Locate every blood parasite and identify its species.
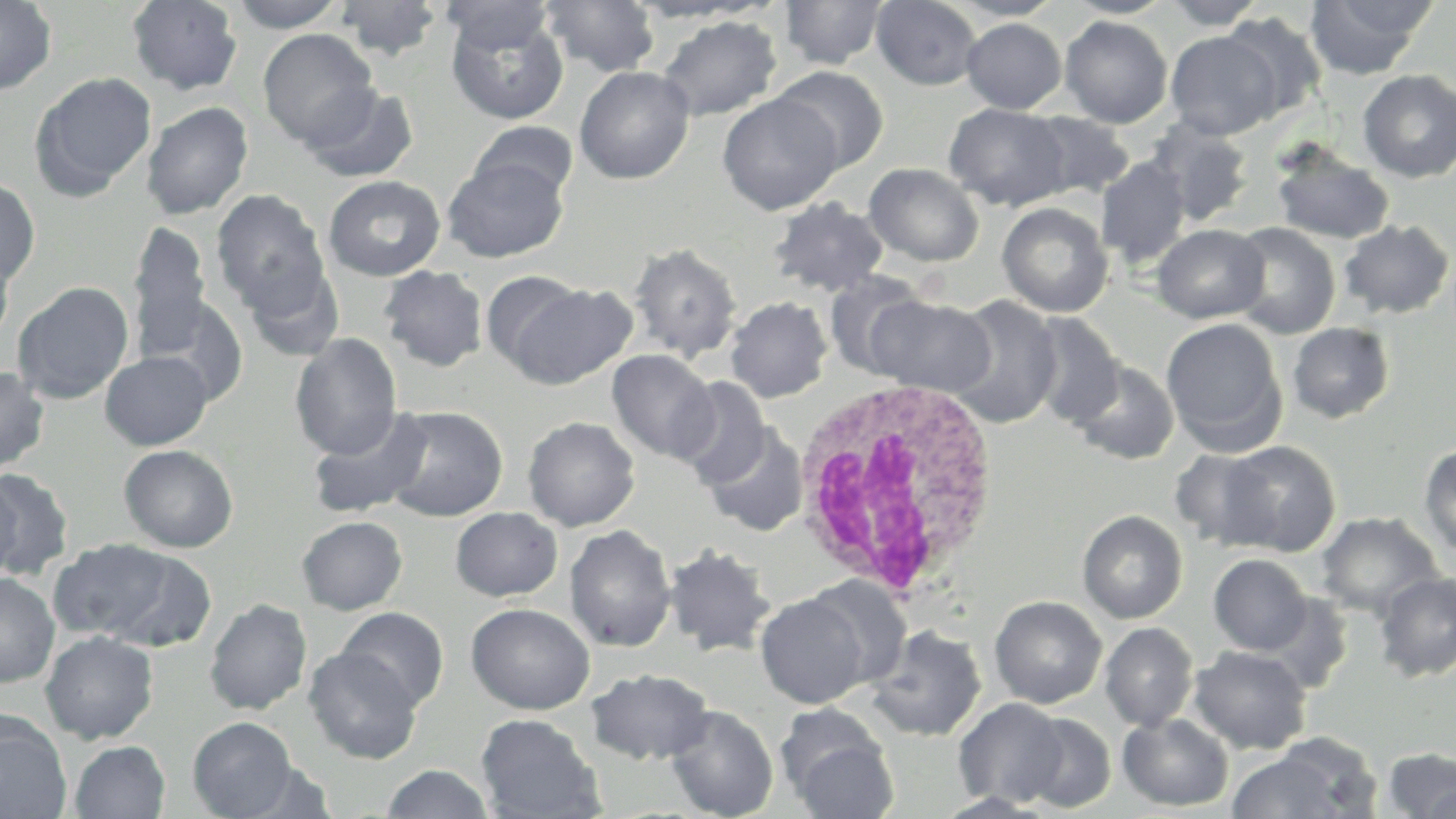
No blood parasites seen.

Summary:
  - Coordinate format: approximate bounding boxes as (x1, y1, x2, y2) in pixels
  - White blood cell locations: (785, 373, 1004, 603)
  - Uninfected red blood cell locations: (0, 0, 57, 95), (126, 0, 244, 96), (440, 0, 556, 54), (779, 0, 889, 69), (871, 0, 983, 90), (946, 0, 1068, 21), (1063, 0, 1177, 19), (1161, 0, 1269, 29), (1304, 0, 1434, 79), (227, 1, 351, 32), (334, 1, 445, 60), (540, 1, 661, 77), (624, 1, 768, 23), (444, 11, 569, 125), (1220, 12, 1328, 124), (656, 16, 782, 122), (1059, 16, 1173, 129), (961, 17, 1067, 114), (258, 28, 379, 148), (1165, 30, 1283, 140), (574, 66, 695, 185), (772, 66, 889, 174), (1357, 69, 1456, 183), (30, 72, 157, 199), (302, 83, 420, 184), (717, 93, 843, 216), (141, 102, 253, 220), (944, 103, 1072, 210), (1025, 112, 1136, 201), (1147, 119, 1255, 228), (468, 121, 578, 203), (1270, 141, 1395, 244), (1096, 156, 1192, 269), (443, 158, 567, 262), (864, 163, 984, 267), (322, 175, 447, 281), (0, 177, 40, 287), (211, 189, 329, 312), (767, 197, 889, 296), (997, 202, 1114, 317), (1339, 219, 1454, 320), (127, 221, 212, 358), (1229, 222, 1341, 340), (1152, 224, 1270, 323), (0, 243, 15, 347), (628, 243, 742, 362), (244, 264, 345, 363), (378, 265, 489, 372), (479, 270, 590, 374), (822, 270, 931, 379), (12, 281, 134, 405), (502, 282, 639, 389), (868, 295, 995, 397), (944, 295, 1063, 429), (143, 296, 249, 404), (725, 296, 833, 403), (1025, 312, 1125, 428), (1161, 317, 1287, 453), (1287, 322, 1395, 423), (290, 333, 402, 461), (606, 349, 718, 463), (100, 351, 213, 450), (1069, 360, 1180, 465), (0, 366, 50, 474), (671, 376, 772, 489), (383, 406, 508, 522), (308, 407, 434, 519), (522, 416, 640, 532), (701, 425, 810, 537), (1219, 440, 1341, 557), (1419, 443, 1456, 559), (119, 444, 239, 552), (1169, 448, 1280, 551), (0, 468, 75, 580), (0, 473, 23, 582), (450, 506, 563, 601), (1077, 510, 1188, 624), (1316, 511, 1444, 619), (296, 516, 408, 615), (565, 524, 676, 652), (48, 539, 187, 643), (661, 544, 777, 658), (1208, 554, 1313, 655), (1374, 570, 1456, 681), (0, 573, 60, 688), (802, 575, 913, 690), (755, 592, 872, 708), (1261, 592, 1356, 692), (989, 596, 1107, 708), (204, 598, 312, 716), (466, 602, 595, 715), (337, 606, 449, 711), (1099, 622, 1199, 731), (866, 625, 988, 742), (40, 631, 159, 744), (1188, 645, 1312, 754), (303, 647, 423, 764), (585, 668, 714, 765), (954, 697, 1069, 809), (665, 705, 779, 819), (1019, 712, 1117, 813), (475, 713, 604, 818), (1117, 713, 1234, 812), (781, 715, 899, 818), (0, 717, 71, 819), (187, 717, 300, 818), (69, 741, 170, 818), (1382, 747, 1456, 818), (1226, 750, 1350, 819), (379, 764, 496, 818)
  - Slide-level diagnosis: no evidence of blood parasites
  - Field of view: one of a larger specimen
  - Preparation: thin blood film
  - Magnification: 1000x
  - Stain: May-Grünwald-Giemsa
  - Image size: 1456×819 pixels
  - Modality: light microscopy